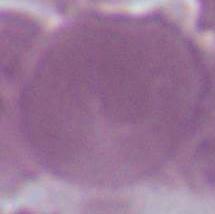 1000x magnification. Photomicrograph. An erythrocyte is shown.